Locate the cells, classifying each as a parasitized red blood cell, an uninfected red blood cell, or a white blood cell.
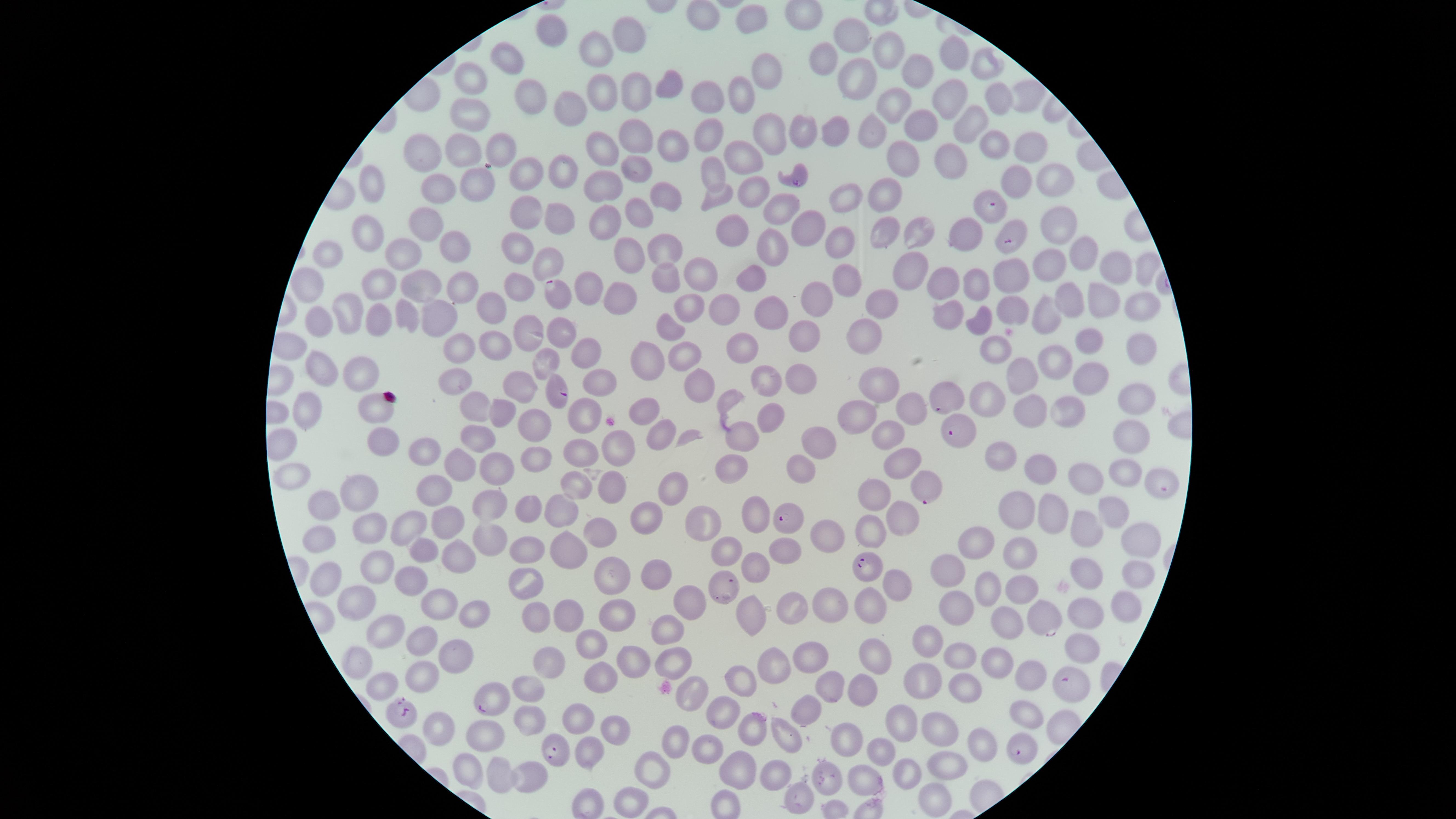
Approximate marker points as (x, y) in pixels.
Parasitized red blood cells: (796, 180), (992, 206), (1010, 237), (559, 291), (556, 390), (950, 398), (956, 429), (1164, 485), (924, 486), (785, 517), (868, 565), (1044, 619), (1069, 685), (487, 700), (402, 711), (556, 749), (1021, 749).
Uninfected red blood cells: (700, 17), (551, 29), (855, 35), (597, 48), (628, 49), (888, 53), (948, 55), (821, 60), (511, 61), (987, 66), (763, 72), (922, 76), (862, 77), (667, 81), (473, 82), (638, 91), (529, 94), (1026, 94), (742, 95), (600, 97), (942, 97), (991, 97), (704, 99), (895, 104), (562, 107), (468, 116), (918, 127), (801, 129), (828, 131), (962, 131), (710, 133), (768, 134), (877, 136), (1032, 137), (641, 139), (499, 144), (994, 145), (468, 147), (603, 148), (665, 150), (428, 155), (899, 156), (745, 160), (945, 162), (557, 167), (525, 171), (637, 174), (709, 174), (1050, 179), (603, 181), (374, 183), (476, 183), (1014, 183), (439, 190), (751, 191), (884, 194), (661, 195), (718, 197), (840, 197), (774, 205), (521, 206), (556, 211), (632, 211), (606, 218), (422, 220), (809, 224), (1055, 224), (736, 230), (923, 230), (968, 230), (365, 231), (886, 234), (838, 239), (520, 243), (772, 244), (457, 245), (664, 249), (627, 252), (405, 253), (1076, 256), (331, 259), (548, 260), (1045, 263), (1139, 266), (1109, 267), (910, 268), (1010, 274), (662, 276), (700, 276), (752, 277), (972, 280), (381, 283), (843, 283), (312, 285), (417, 285), (936, 285), (461, 286), (592, 286), (522, 288), (622, 292), (813, 296), (1068, 299), (1099, 299), (881, 302), (1139, 303), (488, 304), (690, 304), (1014, 307), (407, 309), (714, 309), (772, 309), (950, 311), (350, 312), (1048, 313), (435, 315), (320, 320), (379, 320), (982, 323), (664, 325), (558, 332), (865, 332), (523, 334), (802, 334), (1084, 339), (492, 346), (456, 349), (991, 349), (747, 350), (583, 351), (685, 352), (1134, 353), (649, 355), (1050, 358), (546, 362), (360, 367), (322, 369), (1025, 374), (801, 377), (1086, 377), (449, 378), (596, 378), (765, 380), (879, 384), (698, 385), (516, 388), (1137, 392), (986, 398), (482, 407), (1066, 407), (304, 408), (378, 408), (913, 408), (1023, 410), (504, 411), (643, 411), (767, 415), (855, 416), (584, 421), (535, 428), (662, 431), (738, 433), (883, 433), (483, 434), (1133, 436), (380, 440), (821, 443), (619, 444), (580, 450), (431, 455), (1002, 455), (534, 457), (463, 462), (900, 463), (1037, 464), (731, 465), (499, 466), (801, 468), (1123, 472), (290, 475), (1084, 475), (578, 481), (610, 481), (436, 484), (360, 486), (672, 488), (878, 491), (487, 503), (326, 505), (1019, 505), (1111, 505), (562, 508), (522, 509), (1055, 512), (643, 517), (757, 519), (445, 520), (699, 521), (416, 523), (368, 525), (903, 525), (870, 527), (601, 529), (1085, 529), (825, 531), (490, 533), (319, 537), (978, 538), (1134, 540), (423, 543), (568, 545), (790, 547), (533, 549), (729, 550), (455, 552), (1023, 552), (379, 563), (755, 563), (1089, 565), (952, 569), (656, 574), (1136, 575), (329, 576), (616, 576), (524, 580), (410, 581), (894, 582), (733, 583), (987, 583), (1020, 587), (361, 596), (685, 596), (438, 601), (867, 604), (962, 604), (828, 607), (1126, 607), (566, 608), (792, 608), (469, 610), (745, 610), (1086, 611), (619, 612), (535, 613), (1000, 621), (383, 627), (667, 627), (425, 638), (1085, 641), (930, 643), (593, 646), (452, 649), (805, 653), (668, 655), (868, 655), (964, 656), (629, 659), (355, 660), (550, 662), (998, 665), (421, 667), (775, 667), (1032, 671), (600, 673), (922, 678), (742, 681), (380, 685), (830, 685), (861, 687), (524, 688), (967, 689), (725, 708), (803, 709), (1024, 713), (579, 715), (526, 718), (441, 722), (619, 727), (903, 727), (942, 727), (751, 728), (847, 730), (785, 732), (485, 739), (673, 742), (979, 745), (707, 748), (589, 752), (882, 755), (948, 764), (737, 767), (469, 769), (654, 769), (776, 770), (905, 772), (825, 774), (500, 775), (530, 776), (866, 778), (800, 792), (928, 797), (631, 798).
No white blood cells identified.

Summary:
  - Species: Plasmodium falciparum
  - Capture: smartphone photograph through the microscope eyepiece
  - Stain: Giemsa
  - Field of view: single
  - Visible region: circular
  - Image size: 1456×819 pixels
  - Preparation: thin blood smear